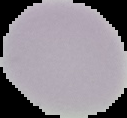

Summary:
  - Result: no Plasmodium parasites detected
  - Image type: segmented cell region on a black background
  - Image size: 127×118 pixels
  - Preparation: thin blood smear